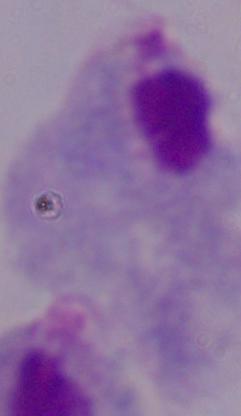
magnification = 1000x
modality = photomicrograph
identification = trichomonad